State which parasite is depicted.
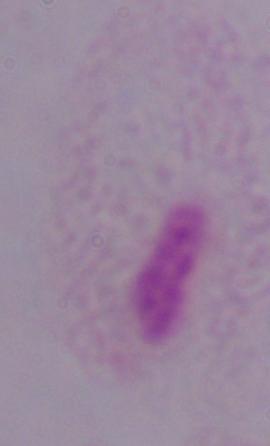
This is a trichomonad.

Photomicrograph. 1000x magnification.